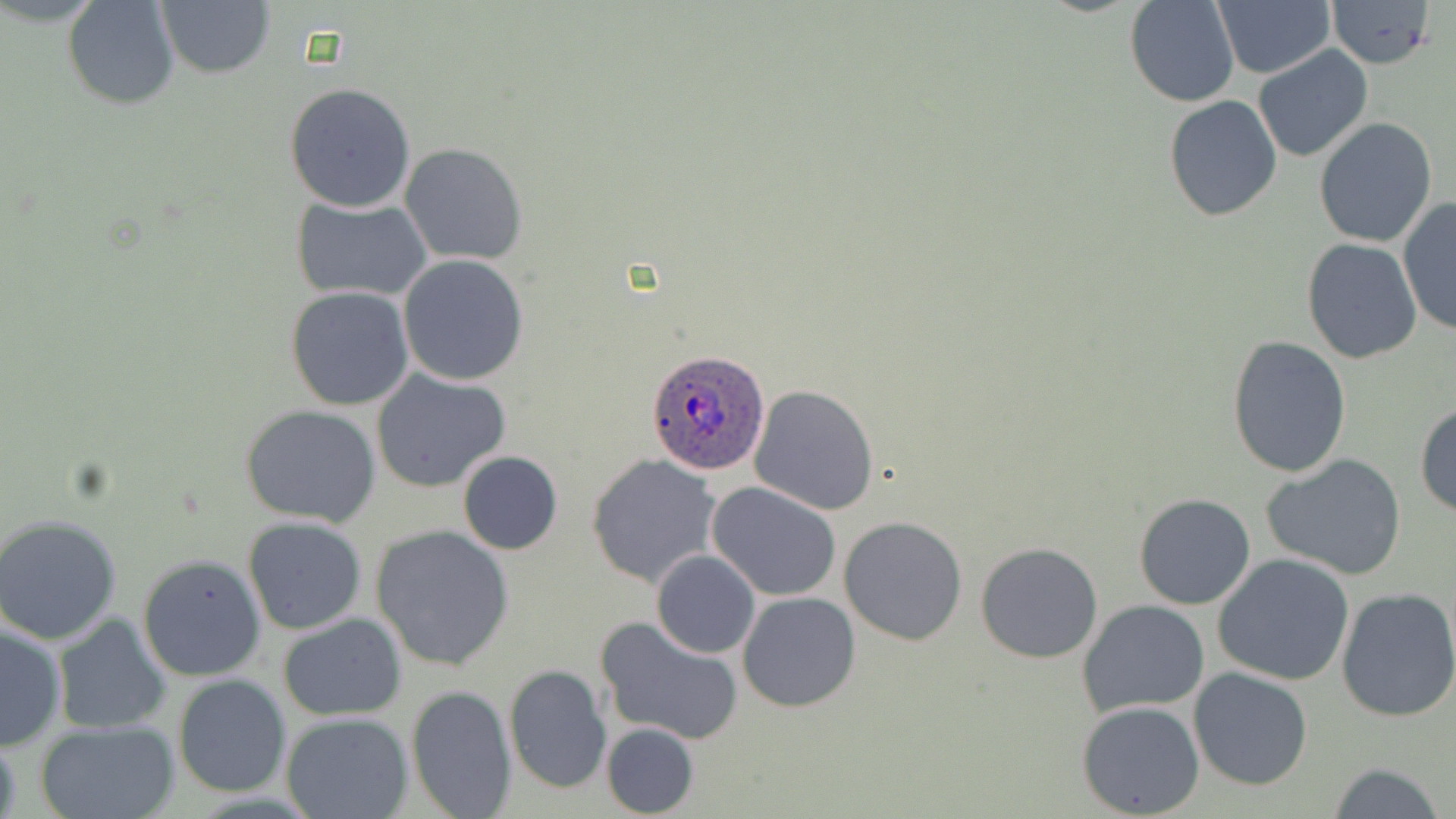

slide-level diagnosis = Plasmodium ovale
field of view = one of a larger specimen
stain = May-Grünwald-Giemsa
image size = 1456×819 pixels
modality = light microscopy
Plasmodium ovale-infected red blood cell locations = approximate bounding boxes as [x1, y1, x2, y2] in pixels: [649, 350, 769, 472]
uninfected red blood cell locations = approximate bounding boxes as [x1, y1, x2, y2] in pixels: [155, 0, 275, 78], [1125, 0, 1241, 107], [1211, 0, 1335, 79], [1329, 0, 1436, 68], [62, 1, 181, 111], [1253, 44, 1373, 162], [285, 82, 417, 213], [1163, 94, 1282, 221], [1312, 117, 1437, 248], [399, 143, 527, 266], [1397, 196, 1456, 336], [292, 197, 432, 303], [1302, 238, 1422, 363], [397, 254, 529, 388], [286, 286, 415, 411], [1227, 336, 1351, 479], [370, 368, 511, 493], [747, 384, 880, 516], [1414, 402, 1456, 518], [242, 405, 381, 527], [457, 451, 563, 555], [1261, 453, 1407, 580], [588, 454, 721, 588], [707, 482, 842, 603], [1134, 493, 1256, 610], [0, 514, 123, 645], [242, 516, 368, 635], [838, 516, 969, 646], [370, 525, 515, 672], [976, 541, 1105, 664], [651, 550, 760, 659], [137, 554, 268, 683], [1212, 554, 1355, 685], [1336, 587, 1456, 723], [736, 591, 860, 712], [1078, 601, 1209, 718], [279, 612, 407, 720], [52, 614, 174, 736], [595, 618, 744, 746], [1, 622, 68, 750], [504, 663, 611, 794], [1190, 668, 1312, 791], [171, 674, 291, 796], [405, 685, 517, 819], [1077, 700, 1205, 817], [282, 713, 412, 819], [32, 719, 181, 819], [601, 722, 698, 818], [0, 738, 23, 819], [1328, 761, 1447, 819]
magnification = 1000x
preparation = thin blood smear